Assess this cell for malaria.
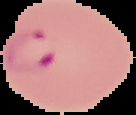
Parasitized.

Summary:
  - Image size: 136×115 pixels
  - Image type: segmented cell region with the area outside set to black
  - Preparation: thin blood smear